Name the cell type shown.
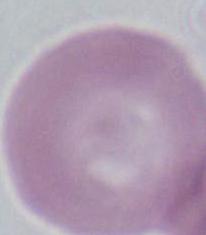

This is an erythrocyte.

magnification = 1000x
modality = photomicrograph